Identify the cell.
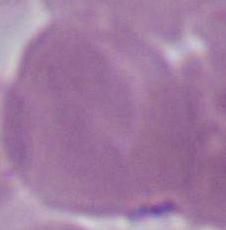
This is an erythrocyte.

modality = photomicrograph
magnification = 1000x